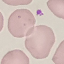
Summary:
  - Result: no malaria parasites detected
  - Image type: automatically extracted cell patch, resized to 64 × 64 pixels
  - Preparation: thin blood smear
  - Stain: Giemsa
  - Capture: smartphone camera at the microscope eyepiece